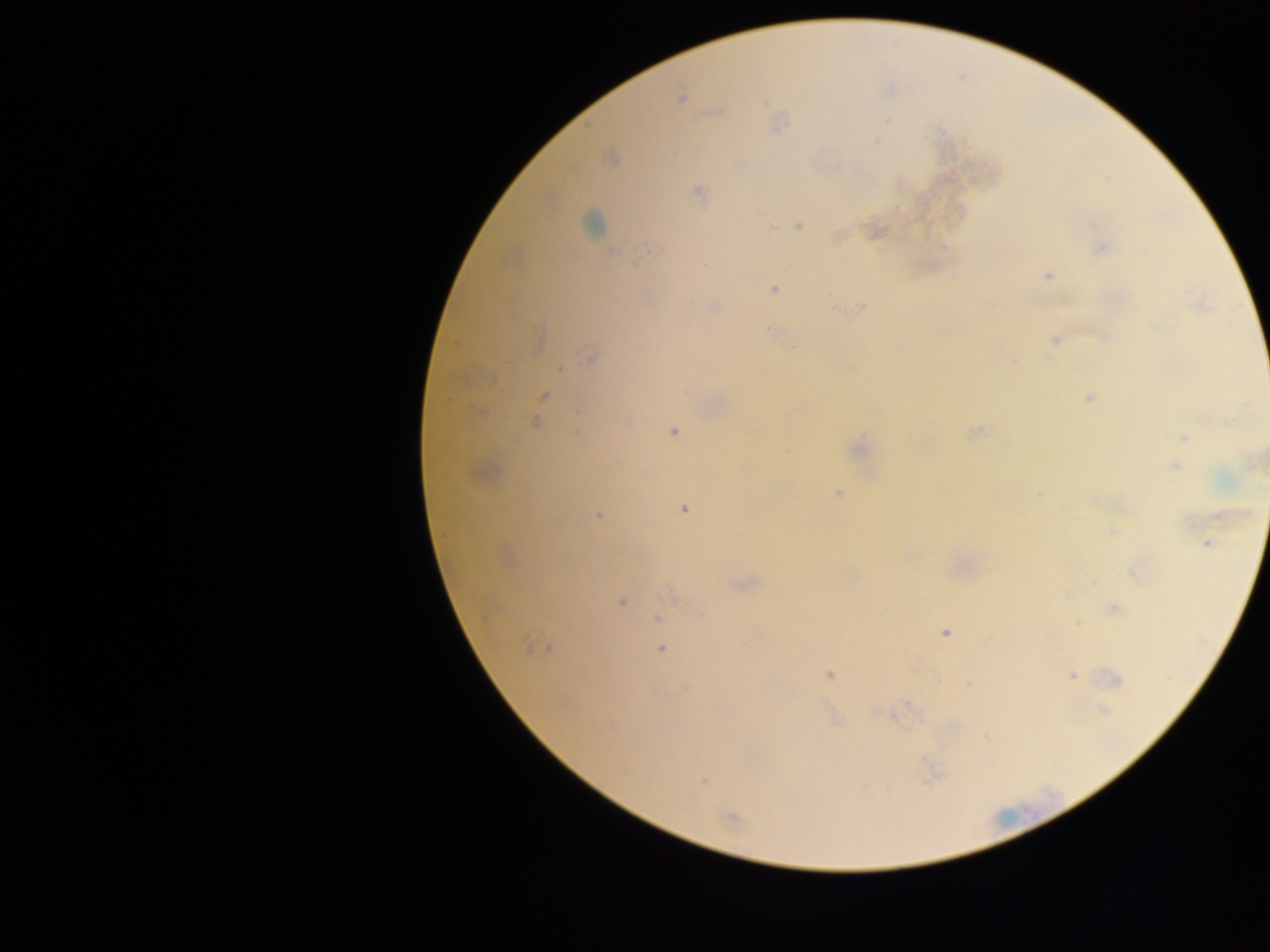

country: Ghana
capture: mobile-phone photograph through a microscope
field_of_view: single
preparation: thick blood film
image_size: 1270×952 pixels
plasmodium_parasite_locations: 'approximate centers as [x, y] in pixels: [680, 99], [875, 141], [611, 158], [697, 192], [798, 226], [771, 227], [1101, 246], [638, 263], [705, 265], [1048, 276], [774, 289], [715, 306], [862, 307], [833, 309], [771, 329], [1104, 337], [1055, 340], [590, 357], [560, 369], [543, 396], [1089, 397], [535, 422], [976, 430], [577, 431], [674, 431], [1185, 437], [857, 448], [1175, 466], [838, 493], [1040, 493], [684, 509], [598, 515], [1113, 532], [1208, 543], [1132, 573], [621, 603], [1114, 608], [658, 619], [945, 633], [529, 648], [551, 649], [662, 649], [829, 674], [1073, 675], [1116, 679], [970, 684], [685, 687], [1104, 710], [837, 722], [704, 781], [731, 817]'
leukocyte_locations: 'approximate centers as [x, y] in pixels: [591, 223]'